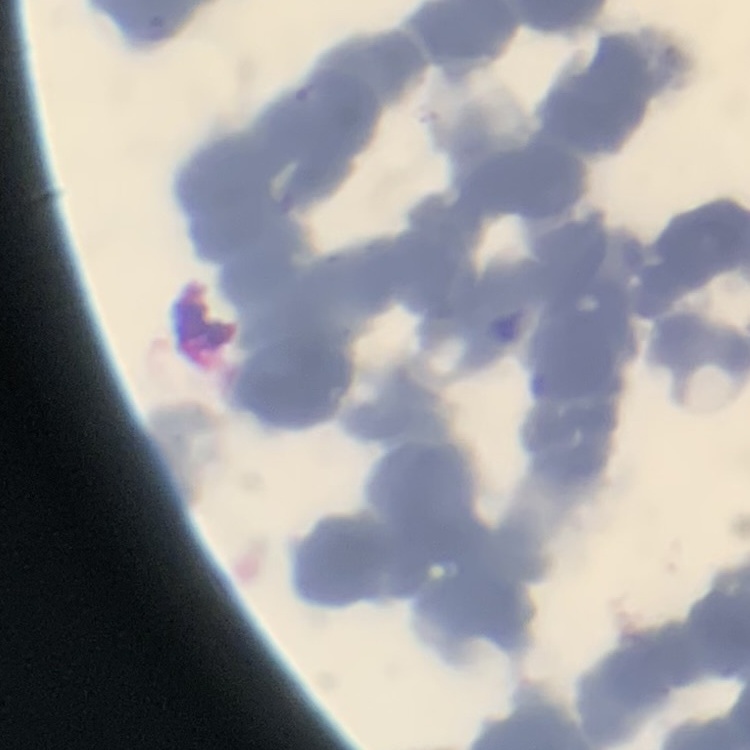

The red blood cells exhibit rouleaux formation. Square crop of a larger photomicrograph. Field's or Giemsa stain. Thin peripheral smear.